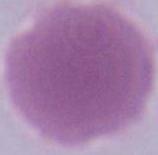
identification = erythrocyte
modality = photomicrograph
magnification = 1000x